State the blood parasite species.
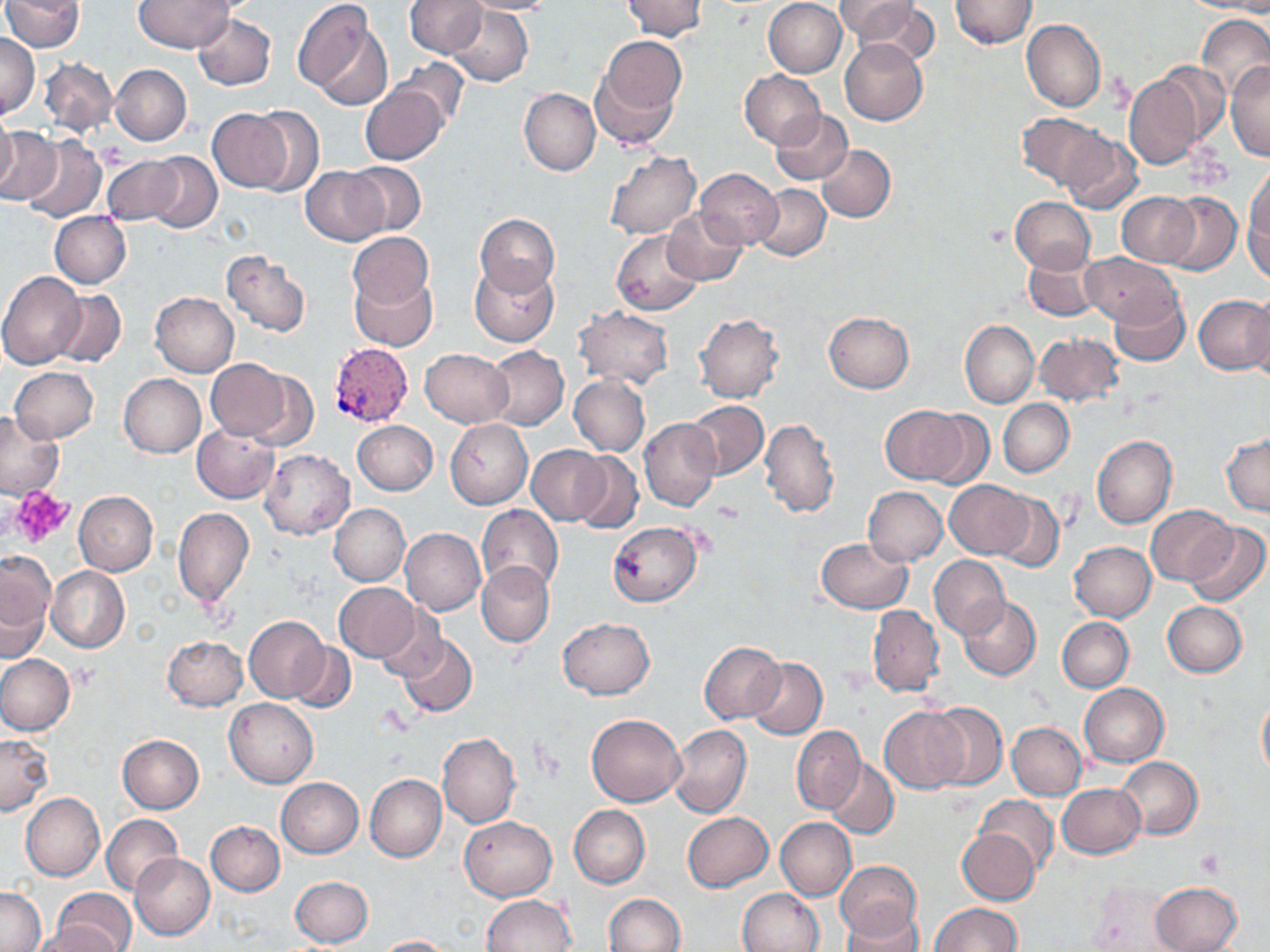
Plasmodium vivax.

preparation = thin blood film
field of view = single
image size = 1270×952 pixels
magnification = 1000x
Plasmodium vivax-infected red blood cell locations = approximate bounding boxes as named x1/y1/x2/y2 corners in pixels: (x1=330, y1=343, x2=412, y2=429)
modality = light microscopy
platelet locations = approximate bounding boxes as named x1/y1/x2/y2 corners in pixels: (x1=7, y1=487, x2=76, y2=548), (x1=714, y1=500, x2=746, y2=525), (x1=70, y1=665, x2=99, y2=691), (x1=1196, y1=848, x2=1225, y2=876)
uninfected red blood cell locations = approximate bounding boxes as named x1/y1/x2/y2 corners in pixels: (x1=134, y1=0, x2=232, y2=52), (x1=406, y1=0, x2=485, y2=57), (x1=461, y1=0, x2=560, y2=15), (x1=623, y1=0, x2=707, y2=41), (x1=835, y1=0, x2=933, y2=53), (x1=949, y1=0, x2=1037, y2=49), (x1=2, y1=1, x2=84, y2=53), (x1=293, y1=1, x2=391, y2=107), (x1=763, y1=1, x2=847, y2=78), (x1=1185, y1=1, x2=1270, y2=14), (x1=445, y1=6, x2=532, y2=88), (x1=1196, y1=13, x2=1270, y2=99), (x1=192, y1=14, x2=275, y2=90), (x1=1021, y1=19, x2=1105, y2=112), (x1=595, y1=33, x2=685, y2=130), (x1=0, y1=35, x2=40, y2=118), (x1=840, y1=39, x2=929, y2=126), (x1=40, y1=56, x2=118, y2=135), (x1=392, y1=60, x2=470, y2=130), (x1=1226, y1=61, x2=1269, y2=160), (x1=109, y1=64, x2=191, y2=146), (x1=1157, y1=64, x2=1229, y2=148), (x1=739, y1=70, x2=825, y2=148), (x1=1122, y1=72, x2=1206, y2=170), (x1=359, y1=83, x2=449, y2=165), (x1=519, y1=88, x2=601, y2=175), (x1=246, y1=106, x2=323, y2=196), (x1=209, y1=108, x2=297, y2=193), (x1=771, y1=109, x2=852, y2=184), (x1=0, y1=112, x2=17, y2=195), (x1=1016, y1=114, x2=1109, y2=191), (x1=0, y1=129, x2=60, y2=207), (x1=1058, y1=132, x2=1142, y2=214), (x1=19, y1=136, x2=106, y2=223), (x1=816, y1=145, x2=895, y2=223), (x1=605, y1=150, x2=701, y2=240), (x1=143, y1=152, x2=222, y2=233), (x1=101, y1=155, x2=184, y2=224), (x1=345, y1=161, x2=426, y2=236), (x1=1244, y1=163, x2=1270, y2=270), (x1=300, y1=166, x2=389, y2=244), (x1=695, y1=168, x2=783, y2=249), (x1=753, y1=185, x2=830, y2=260), (x1=1117, y1=192, x2=1200, y2=266), (x1=1161, y1=193, x2=1241, y2=275), (x1=1009, y1=196, x2=1096, y2=274), (x1=661, y1=210, x2=747, y2=286), (x1=50, y1=211, x2=131, y2=287), (x1=475, y1=213, x2=560, y2=295), (x1=347, y1=231, x2=433, y2=312), (x1=612, y1=231, x2=705, y2=315), (x1=1024, y1=249, x2=1102, y2=321), (x1=220, y1=250, x2=311, y2=337), (x1=1082, y1=252, x2=1179, y2=325), (x1=469, y1=260, x2=559, y2=347), (x1=0, y1=271, x2=85, y2=369), (x1=351, y1=271, x2=436, y2=350), (x1=50, y1=290, x2=126, y2=367), (x1=150, y1=291, x2=239, y2=377), (x1=1109, y1=291, x2=1189, y2=368), (x1=1194, y1=294, x2=1270, y2=375), (x1=1246, y1=295, x2=1270, y2=388), (x1=573, y1=306, x2=674, y2=388), (x1=823, y1=312, x2=914, y2=392), (x1=694, y1=313, x2=783, y2=403), (x1=960, y1=320, x2=1038, y2=407), (x1=1034, y1=332, x2=1125, y2=407), (x1=484, y1=345, x2=568, y2=430), (x1=420, y1=348, x2=513, y2=427), (x1=209, y1=360, x2=303, y2=445), (x1=9, y1=366, x2=99, y2=443), (x1=119, y1=374, x2=205, y2=458), (x1=569, y1=374, x2=649, y2=456), (x1=998, y1=399, x2=1074, y2=476), (x1=686, y1=400, x2=768, y2=480), (x1=880, y1=404, x2=969, y2=485), (x1=0, y1=409, x2=67, y2=502), (x1=920, y1=410, x2=995, y2=487), (x1=640, y1=417, x2=720, y2=511), (x1=760, y1=418, x2=840, y2=518), (x1=446, y1=419, x2=532, y2=509), (x1=352, y1=420, x2=438, y2=496), (x1=192, y1=425, x2=280, y2=503), (x1=1091, y1=434, x2=1177, y2=529), (x1=1221, y1=434, x2=1270, y2=516), (x1=529, y1=447, x2=609, y2=526), (x1=259, y1=449, x2=355, y2=540), (x1=570, y1=450, x2=642, y2=533), (x1=946, y1=480, x2=1031, y2=557), (x1=863, y1=486, x2=947, y2=566), (x1=74, y1=491, x2=157, y2=576), (x1=989, y1=492, x2=1064, y2=572), (x1=329, y1=504, x2=409, y2=585), (x1=477, y1=505, x2=563, y2=595), (x1=1146, y1=505, x2=1237, y2=585), (x1=173, y1=509, x2=254, y2=607), (x1=608, y1=522, x2=701, y2=607), (x1=1186, y1=524, x2=1269, y2=606), (x1=400, y1=528, x2=486, y2=615), (x1=815, y1=538, x2=913, y2=614), (x1=1069, y1=542, x2=1156, y2=621), (x1=0, y1=549, x2=56, y2=659), (x1=930, y1=555, x2=1010, y2=639), (x1=477, y1=561, x2=554, y2=647), (x1=47, y1=566, x2=129, y2=652), (x1=335, y1=583, x2=422, y2=662), (x1=957, y1=596, x2=1041, y2=680), (x1=1163, y1=602, x2=1246, y2=677), (x1=867, y1=605, x2=943, y2=697), (x1=372, y1=607, x2=443, y2=680), (x1=244, y1=616, x2=329, y2=703), (x1=1057, y1=617, x2=1133, y2=692), (x1=558, y1=618, x2=655, y2=699), (x1=397, y1=633, x2=477, y2=718), (x1=162, y1=635, x2=248, y2=711), (x1=699, y1=640, x2=785, y2=723), (x1=289, y1=642, x2=356, y2=715), (x1=0, y1=653, x2=75, y2=734), (x1=747, y1=658, x2=828, y2=738), (x1=1078, y1=683, x2=1168, y2=767), (x1=1257, y1=692, x2=1270, y2=781), (x1=225, y1=698, x2=317, y2=787), (x1=925, y1=702, x2=1007, y2=790), (x1=880, y1=707, x2=966, y2=793), (x1=587, y1=714, x2=686, y2=805), (x1=1007, y1=721, x2=1087, y2=800), (x1=668, y1=724, x2=751, y2=818), (x1=791, y1=726, x2=864, y2=813), (x1=0, y1=733, x2=52, y2=815), (x1=438, y1=733, x2=521, y2=827), (x1=119, y1=735, x2=204, y2=812), (x1=1116, y1=757, x2=1202, y2=838), (x1=825, y1=759, x2=899, y2=839), (x1=365, y1=774, x2=447, y2=862), (x1=276, y1=778, x2=364, y2=857), (x1=1057, y1=784, x2=1145, y2=858), (x1=21, y1=793, x2=105, y2=882), (x1=976, y1=795, x2=1059, y2=873), (x1=569, y1=804, x2=650, y2=888), (x1=681, y1=812, x2=772, y2=892), (x1=102, y1=814, x2=182, y2=896), (x1=460, y1=817, x2=556, y2=901), (x1=775, y1=817, x2=856, y2=901), (x1=205, y1=821, x2=285, y2=896), (x1=957, y1=829, x2=1039, y2=905), (x1=130, y1=853, x2=214, y2=939), (x1=834, y1=861, x2=921, y2=942), (x1=290, y1=876, x2=373, y2=948), (x1=1084, y1=880, x2=1188, y2=949), (x1=1150, y1=881, x2=1241, y2=952), (x1=0, y1=886, x2=44, y2=951), (x1=51, y1=887, x2=138, y2=952), (x1=739, y1=888, x2=824, y2=952), (x1=604, y1=893, x2=685, y2=952), (x1=481, y1=894, x2=575, y2=952), (x1=932, y1=903, x2=1022, y2=952), (x1=841, y1=907, x2=926, y2=952), (x1=30, y1=925, x2=119, y2=952), (x1=374, y1=935, x2=458, y2=952)
stain = May-Grünwald-Giemsa